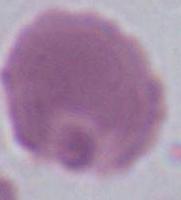

magnification = 1000x
identification = erythrocyte
modality = micrograph